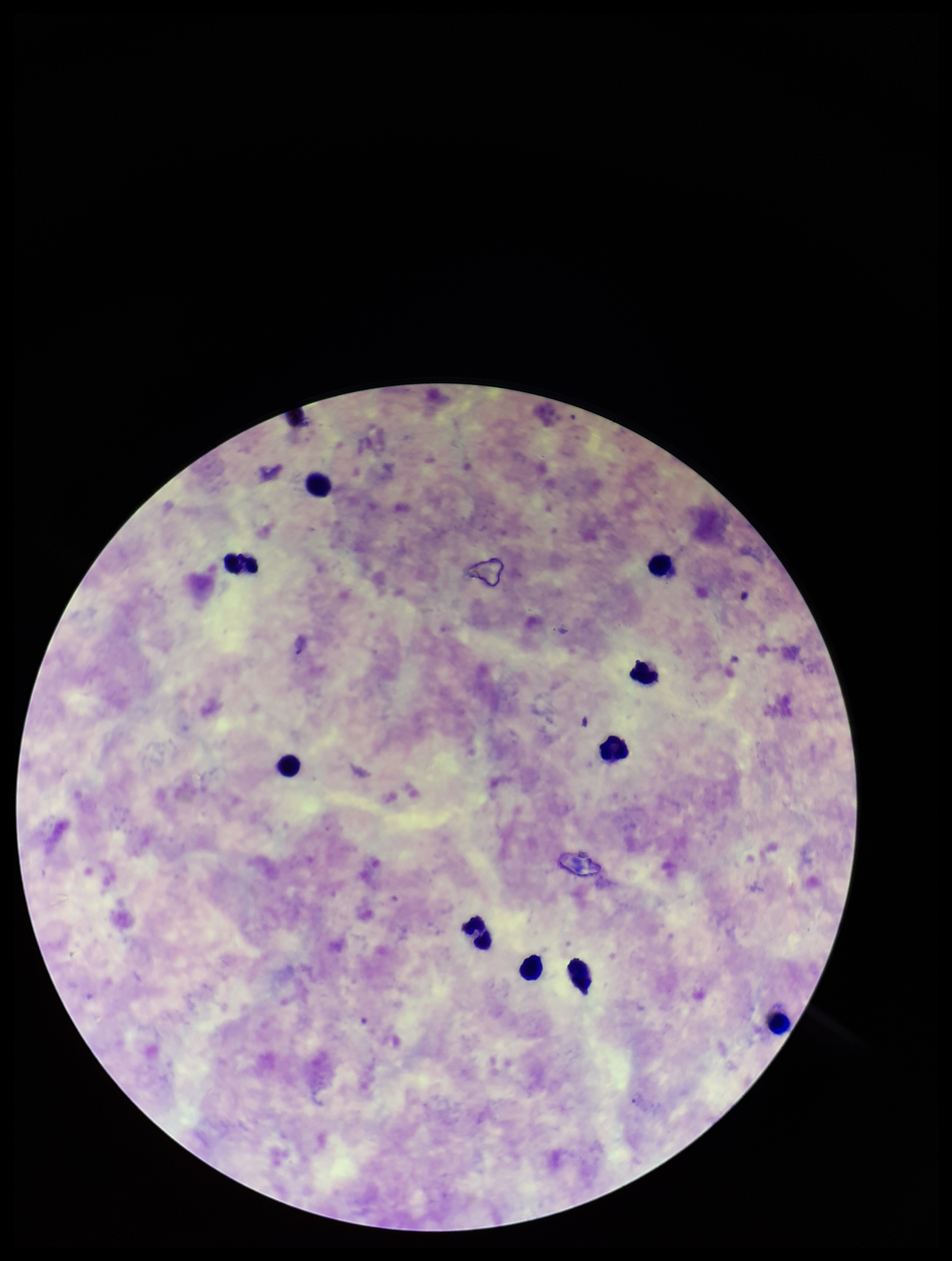
Summary:
  - Preparation: thick smear
  - Plasmodium parasites: seen
  - Image size: 952×1261 pixels
  - Capture: smartphone photograph through the microscope eyepiece
  - Field of view: one from this slide
  - Stain: Giemsa
  - Leukocyte count: 10
  - Species reported for this patient: Plasmodium vivax
  - Parasite count: 1
  - Patient malaria status: infected